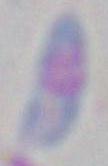

Toxoplasma gondii is shown. Photomicrograph. 1000x magnification.